Report the malaria status of this cell.
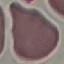

It is uninfected.

capture: smartphone through the microscope eyepiece
stain: Giemsa
preparation: thin blood film
image_type: cell patch, automatically extracted from a larger field of view and resized to 64 × 64 pixels